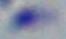
Summary:
  - Magnification: 1000x
  - Identification: Toxoplasma gondii
  - Modality: micrograph